Assess the morphology of the erythrocytes.
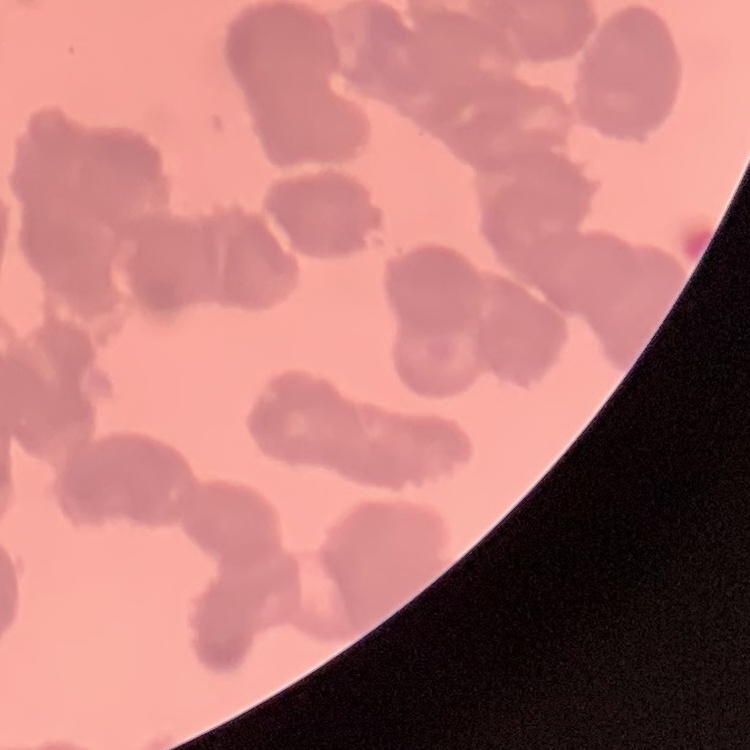
They show rouleaux formation.

preparation = thin blood smear
stain = Field's or Giemsa
image type = one tile cut from a larger photomicrograph